State which parasite is depicted.
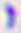
Toxoplasma gondii.

Summary:
  - Magnification: 400x
  - Modality: micrograph